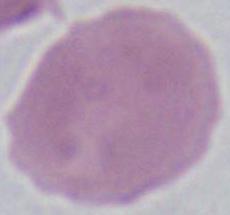

Summary:
  - Modality: micrograph
  - Identification: erythrocyte
  - Magnification: 1000x